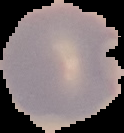 Image is 124×133 pixels. From a thin blood film. The area outside the segmented cell region is set to black. Malaria status: parasitized.